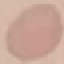
{
  "result": "no malaria parasites detected",
  "capture": "smartphone camera at the microscope eyepiece",
  "image_type": "cell patch, automatically extracted from a larger field of view and resized to 64 × 64 pixels",
  "stain": "Giemsa",
  "preparation": "thin blood smear"
}